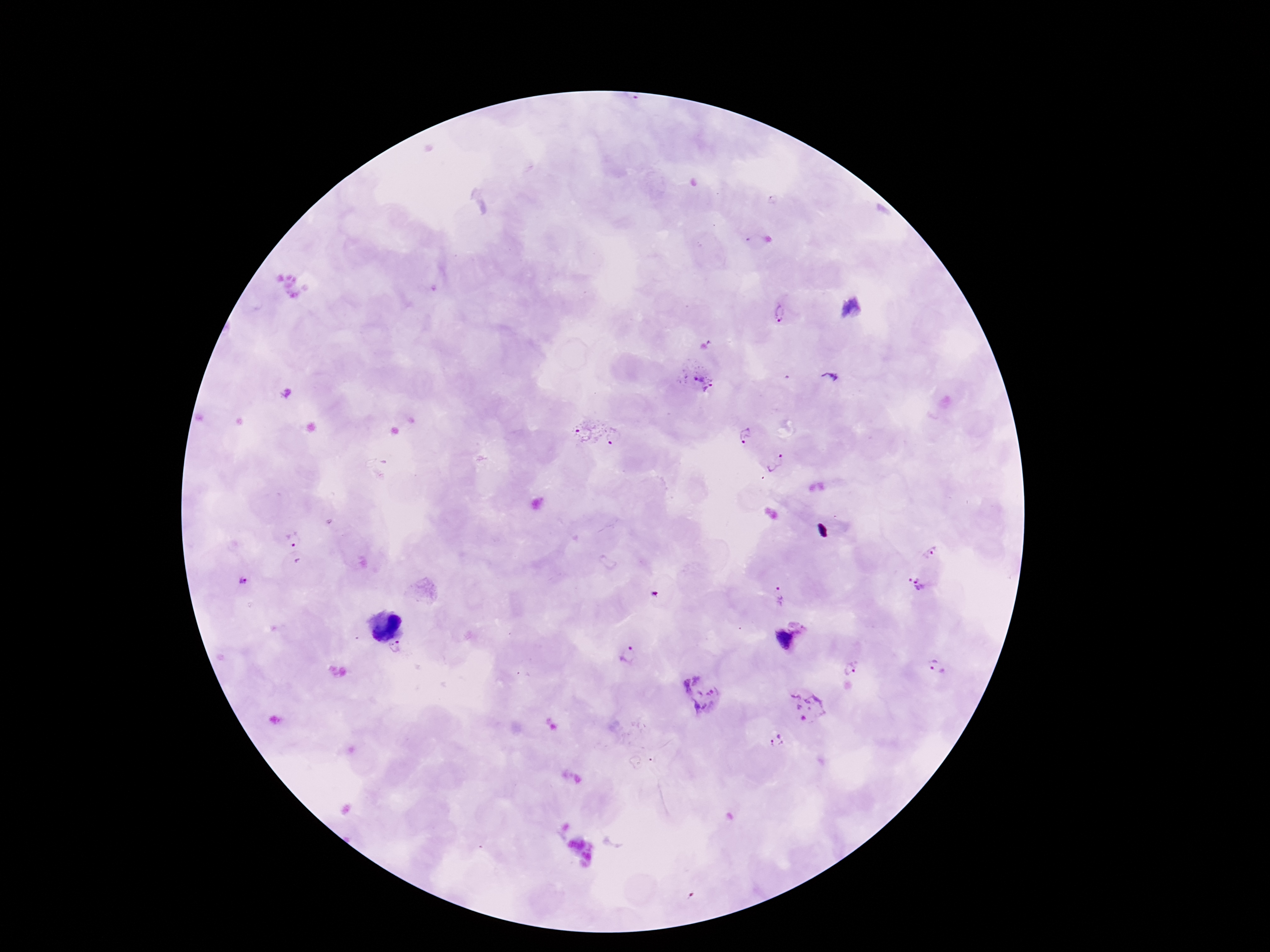

Approximate centers as (x, y) in pixels.
Summary:
  - Plasmodium parasite locations: (782, 314), (830, 374), (700, 376), (582, 429), (747, 436), (614, 437), (775, 462), (295, 541), (932, 550), (244, 581), (916, 586), (780, 595), (788, 639), (395, 649), (629, 655), (934, 665), (850, 666), (705, 692), (807, 707), (775, 742)
  - Stain: Giemsa
  - Image size: 1270×952 pixels
  - Field of view: one from this slide
  - Capture: smartphone camera through the microscope eyepiece
  - Magnification: 100x
  - Preparation: thick peripheral-blood smear
  - Patient malaria status: positive